Report the malaria status of this cell.
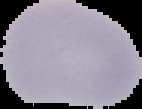
Uninfected.

Summary:
  - Image type: segmented cell region on a black background
  - Image size: 142×109 pixels
  - Preparation: thin blood film